Locate every Plasmodium falciparum-infected red blood cell.
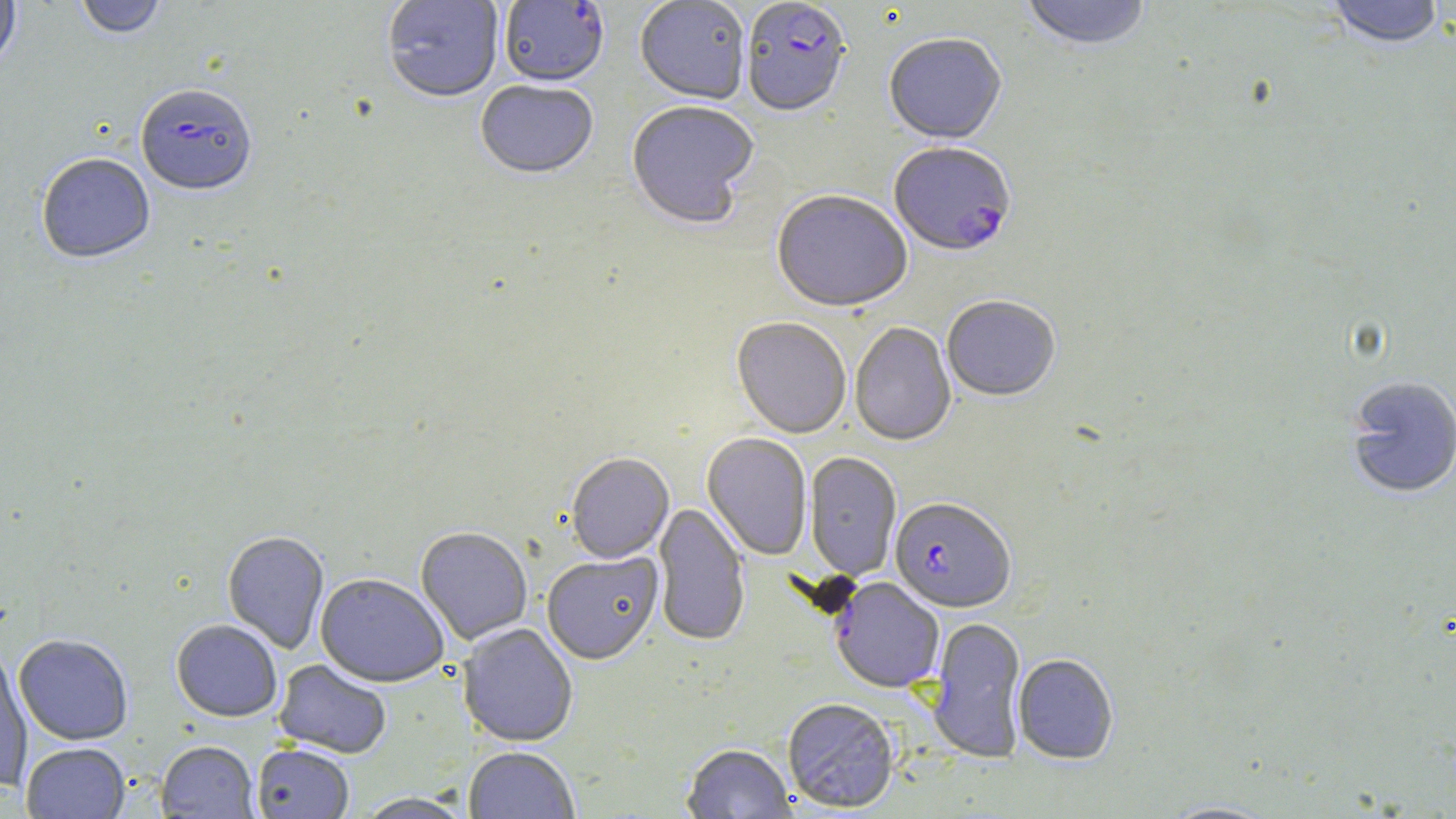

Approximate bounding boxes as (x1, y1, x2, y2) in pixels.
Plasmodium falciparum-infected red blood cells (subset): (742, 1, 851, 120), (135, 86, 257, 199), (889, 144, 1016, 259), (890, 497, 1016, 613).

Uninfected red blood cell locations (subset): (0, 0, 20, 73), (74, 0, 166, 40), (382, 0, 504, 105), (635, 0, 750, 106), (1020, 0, 1152, 54), (1324, 1, 1444, 51), (884, 35, 1007, 147), (475, 82, 598, 182), (626, 103, 759, 231), (36, 155, 155, 266), (771, 192, 912, 315), (942, 297, 1060, 403), (732, 318, 851, 440), (850, 323, 956, 448), (1344, 376, 1456, 500), (702, 433, 812, 561), (804, 452, 902, 581), (565, 454, 673, 565), (654, 503, 750, 647), (416, 528, 532, 646), (222, 532, 329, 654), (542, 552, 663, 666), (315, 574, 449, 687), (830, 577, 944, 693), (927, 617, 1027, 763), (171, 619, 283, 722), (458, 623, 578, 748), (14, 634, 133, 745), (0, 645, 33, 791), (1013, 654, 1119, 765), (273, 660, 392, 758), (783, 699, 900, 813), (156, 741, 259, 818), (22, 742, 130, 818), (682, 743, 796, 818), (252, 744, 354, 818), (464, 747, 579, 819), (355, 792, 475, 818), (1159, 800, 1282, 818). Slide-level diagnosis: Plasmodium falciparum. Thin blood film. 1000x magnification. Light microscopy. Image is 1456×819 pixels. May-Grünwald-Giemsa-stained preparation. Single field of view.